Identify the parasite.
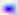
This is Toxoplasma gondii.

Summary:
  - Modality: micrograph
  - Magnification: 400x